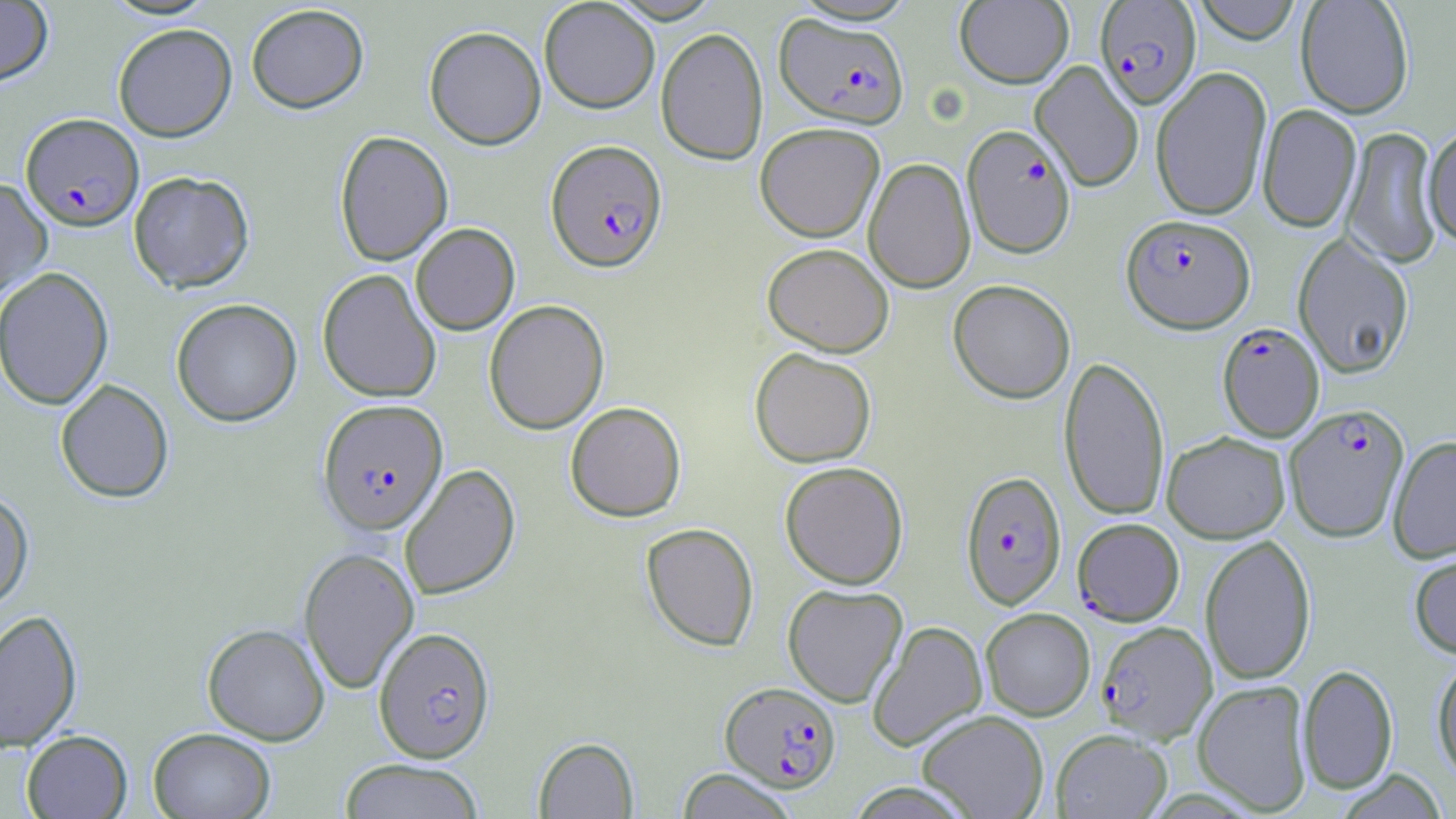
Approximate bounding boxes as [x1, y1, x2, y2] in pixels. Plasmodium falciparum-infected red blood cell locations: [1094, 1, 1202, 110], [774, 12, 910, 128], [21, 113, 144, 231], [962, 125, 1076, 259], [546, 140, 667, 272], [1121, 214, 1255, 333], [1217, 322, 1325, 442], [318, 399, 448, 535], [1285, 403, 1410, 542], [960, 470, 1066, 610], [1070, 524, 1182, 632], [1097, 621, 1217, 744], [373, 627, 496, 763], [720, 681, 841, 792]. Uninfected red blood cell locations: [101, 0, 220, 21], [539, 0, 660, 113], [1191, 0, 1304, 45], [1295, 0, 1415, 119], [0, 1, 54, 86], [954, 1, 1074, 88], [246, 4, 369, 113], [112, 23, 237, 142], [424, 25, 546, 149], [656, 27, 768, 165], [1030, 61, 1144, 192], [1151, 67, 1273, 221], [1257, 105, 1362, 233], [755, 122, 885, 242], [1342, 126, 1444, 269], [1423, 126, 1456, 251], [334, 130, 453, 266], [863, 157, 976, 293], [128, 171, 255, 292], [0, 178, 52, 301], [410, 222, 520, 335], [1292, 233, 1415, 378], [762, 242, 894, 356], [0, 266, 114, 410], [318, 269, 441, 403], [948, 279, 1076, 404], [171, 298, 302, 427], [484, 299, 609, 434], [749, 347, 877, 468], [1059, 355, 1170, 522], [55, 379, 174, 503], [565, 401, 686, 521], [1162, 431, 1291, 543], [1388, 435, 1456, 563], [779, 461, 909, 589], [400, 464, 521, 600], [0, 488, 34, 613], [641, 522, 759, 651], [1200, 535, 1316, 685], [298, 546, 419, 694], [1409, 549, 1456, 659], [782, 583, 908, 707], [981, 608, 1095, 721], [0, 610, 82, 752], [867, 621, 987, 752], [202, 624, 329, 745], [1432, 656, 1456, 783], [1298, 664, 1398, 795], [1192, 679, 1313, 814], [917, 710, 1048, 819], [148, 727, 276, 818], [1051, 729, 1172, 818], [21, 730, 133, 818], [533, 736, 639, 818], [340, 758, 486, 819], [676, 768, 798, 818], [1334, 770, 1449, 818], [844, 782, 979, 818]. Slide-level diagnosis: Plasmodium falciparum. May-Grünwald-Giemsa-stained preparation. Light microscopy. Image is 1456×819 pixels. Single field of view. Thin blood film. Captured at 1000x magnification.